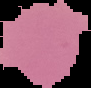
preparation = thin blood smear
result = no Plasmodium parasites seen
image type = cell region segmented out of the field of view; surrounding area masked to black
image size = 91×88 pixels